Classify this cell by malaria status.
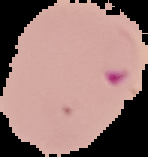

Parasitized.

Image is 148×157 pixels. From a thin blood film. Cell region segmented out of the field of view; the surrounding area is masked to black.